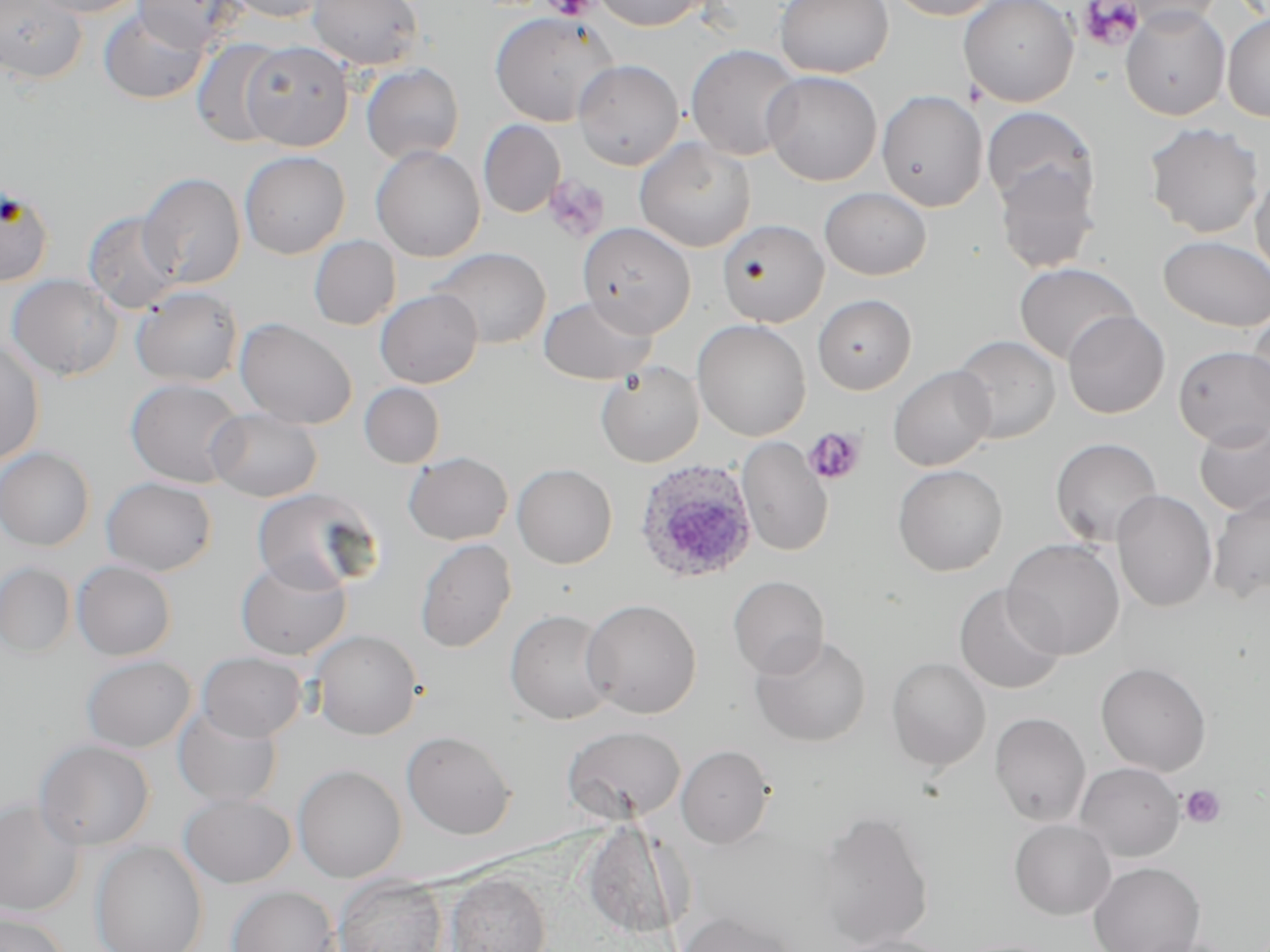

Summary:
  - Coordinate format: approximate bounding boxes as (x1, y1, x2, y2) in pixels
  - Plasmodium ovale-infected red blood cell locations: (632, 457, 759, 585)
  - Platelet locations: (544, 0, 599, 21), (1077, 0, 1144, 51), (543, 174, 610, 242), (803, 427, 867, 486), (1181, 785, 1226, 828)
  - Uninfected red blood cell locations: (0, 0, 87, 84), (27, 0, 145, 18), (133, 0, 243, 52), (224, 0, 331, 23), (307, 0, 423, 70), (592, 0, 710, 30), (775, 0, 893, 78), (885, 0, 1004, 20), (958, 0, 1079, 107), (1111, 0, 1224, 32), (1121, 6, 1230, 121), (99, 7, 210, 105), (489, 11, 620, 127), (1222, 12, 1270, 122), (191, 37, 287, 146), (241, 41, 354, 151), (685, 44, 803, 161), (573, 59, 684, 170), (361, 63, 464, 164), (762, 70, 882, 186), (877, 90, 988, 211), (982, 106, 1098, 214), (479, 120, 565, 218), (1144, 122, 1265, 238), (634, 138, 757, 252), (371, 145, 485, 262), (240, 150, 350, 259), (993, 164, 1099, 273), (1251, 167, 1270, 286), (138, 172, 246, 289), (0, 184, 55, 286), (819, 187, 931, 280), (83, 211, 182, 314), (717, 219, 829, 328), (577, 221, 696, 337), (308, 235, 401, 330), (1159, 235, 1270, 331), (429, 247, 551, 350), (1014, 262, 1139, 365), (6, 274, 123, 381), (130, 286, 244, 388), (375, 289, 483, 388), (812, 294, 916, 395), (538, 296, 657, 385), (1062, 310, 1170, 419), (1246, 310, 1270, 418), (235, 318, 357, 429), (692, 319, 811, 440), (951, 335, 1061, 444), (0, 340, 46, 465), (1174, 345, 1270, 448), (596, 361, 704, 467), (888, 366, 996, 471), (125, 377, 247, 488), (359, 382, 445, 468), (207, 408, 323, 502), (1193, 420, 1270, 516), (737, 437, 833, 557), (1050, 437, 1163, 547), (0, 446, 95, 551), (403, 452, 512, 545), (512, 464, 617, 569), (892, 464, 1008, 576), (101, 477, 217, 576), (252, 487, 380, 593), (1111, 489, 1217, 612), (1207, 489, 1270, 604), (415, 538, 516, 653), (1002, 538, 1124, 659), (235, 556, 352, 660), (71, 560, 177, 660), (0, 563, 75, 656), (728, 575, 830, 678), (954, 583, 1066, 695), (581, 598, 702, 718), (505, 609, 617, 725), (309, 629, 422, 740), (749, 632, 873, 748), (197, 651, 307, 742), (81, 655, 197, 753), (886, 657, 991, 771), (1095, 661, 1212, 776), (173, 704, 283, 808), (989, 712, 1091, 827), (562, 724, 686, 825), (401, 730, 517, 840), (34, 739, 155, 851), (676, 744, 775, 849), (1075, 762, 1185, 862), (292, 764, 407, 882), (178, 794, 295, 888), (0, 796, 86, 917), (811, 809, 934, 949), (1009, 818, 1116, 920), (581, 820, 688, 941), (90, 841, 208, 952), (1088, 861, 1205, 952), (446, 873, 551, 952), (333, 874, 449, 952), (226, 885, 340, 952), (0, 911, 70, 952), (676, 911, 802, 952), (827, 934, 960, 952)
  - Slide-level diagnosis: Plasmodium ovale
  - Stain: May-Grünwald-Giemsa
  - Magnification: 1000x
  - Image size: 1270×952 pixels
  - Preparation: thin blood film
  - Modality: light microscopy
  - Field of view: single